Report the malaria status of this cell.
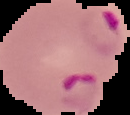

It is parasitized.

image size = 130×115 pixels
image type = segmented cell region with the area outside set to black
preparation = thin blood smear